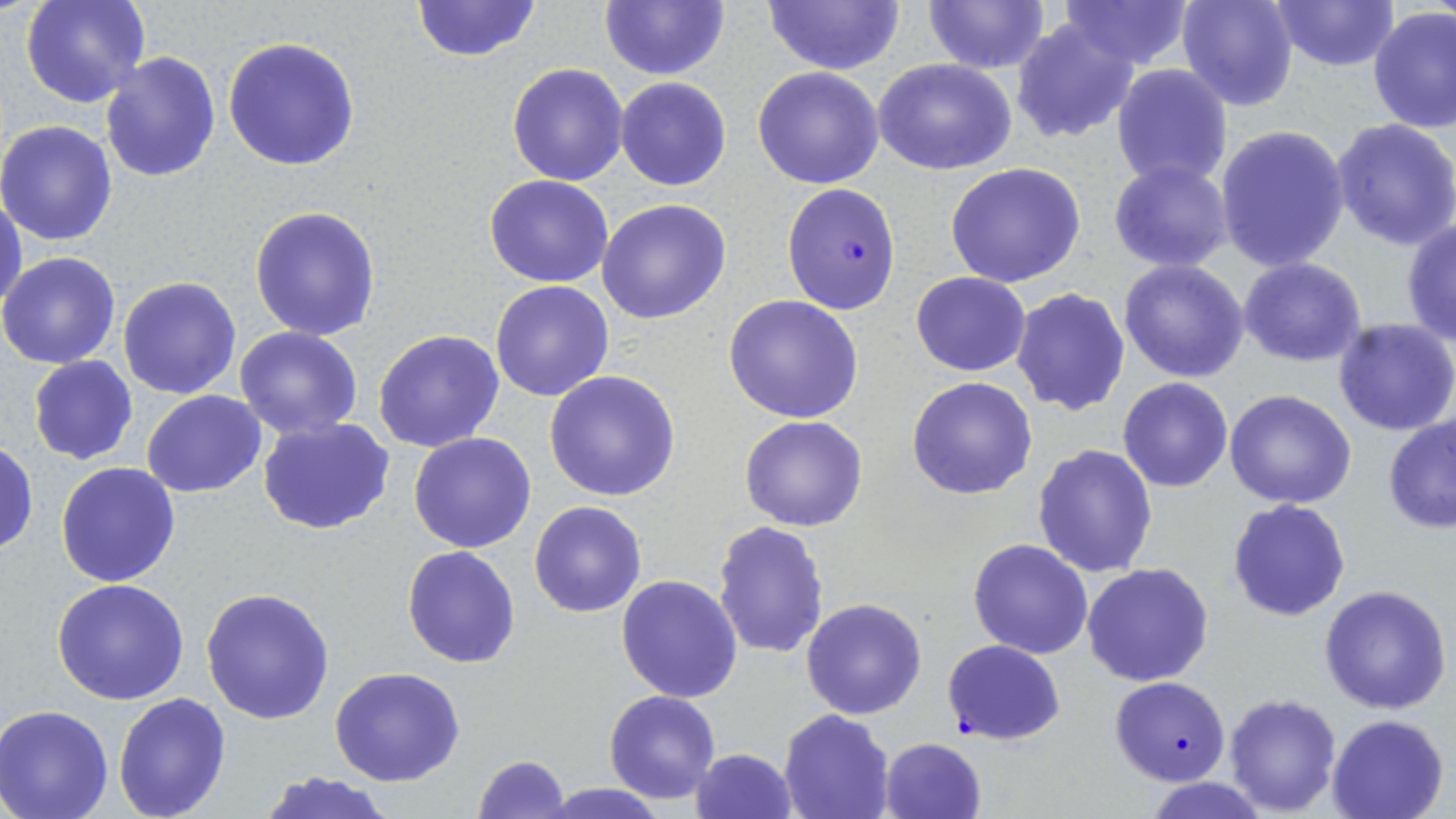
Approximate bounding boxes as named x1/y1/x2/y2 corners in pixels. Uninfected red blood cell locations: (x1=21, y1=0, x2=149, y2=108), (x1=598, y1=0, x2=731, y2=82), (x1=759, y1=0, x2=907, y2=74), (x1=924, y1=0, x2=1052, y2=73), (x1=1054, y1=0, x2=1196, y2=71), (x1=1176, y1=0, x2=1298, y2=112), (x1=1266, y1=0, x2=1402, y2=71), (x1=409, y1=1, x2=545, y2=61), (x1=1369, y1=7, x2=1456, y2=134), (x1=1011, y1=17, x2=1140, y2=144), (x1=223, y1=37, x2=362, y2=172), (x1=99, y1=52, x2=221, y2=182), (x1=873, y1=57, x2=1016, y2=176), (x1=507, y1=61, x2=631, y2=184), (x1=1112, y1=63, x2=1233, y2=189), (x1=753, y1=65, x2=885, y2=188), (x1=615, y1=76, x2=732, y2=192), (x1=1330, y1=118, x2=1456, y2=250), (x1=0, y1=119, x2=120, y2=246), (x1=1215, y1=124, x2=1350, y2=272), (x1=1107, y1=159, x2=1235, y2=272), (x1=945, y1=162, x2=1087, y2=287), (x1=484, y1=174, x2=615, y2=288), (x1=0, y1=189, x2=27, y2=316), (x1=597, y1=198, x2=732, y2=324), (x1=250, y1=206, x2=383, y2=342), (x1=1401, y1=217, x2=1456, y2=346), (x1=0, y1=251, x2=122, y2=368), (x1=1239, y1=256, x2=1367, y2=367), (x1=1118, y1=258, x2=1251, y2=383), (x1=911, y1=272, x2=1031, y2=376), (x1=118, y1=276, x2=242, y2=400), (x1=490, y1=281, x2=614, y2=402), (x1=1011, y1=287, x2=1131, y2=416), (x1=723, y1=295, x2=864, y2=424), (x1=1333, y1=318, x2=1456, y2=437), (x1=234, y1=327, x2=364, y2=441), (x1=373, y1=328, x2=505, y2=453), (x1=28, y1=356, x2=138, y2=464), (x1=544, y1=370, x2=681, y2=502), (x1=907, y1=376, x2=1039, y2=499), (x1=1118, y1=376, x2=1233, y2=492), (x1=1225, y1=389, x2=1357, y2=510), (x1=142, y1=390, x2=266, y2=496), (x1=1382, y1=413, x2=1456, y2=533), (x1=739, y1=414, x2=869, y2=531), (x1=257, y1=417, x2=395, y2=536), (x1=408, y1=433, x2=537, y2=553), (x1=1, y1=438, x2=38, y2=557), (x1=1033, y1=443, x2=1160, y2=578), (x1=56, y1=462, x2=181, y2=587), (x1=1227, y1=498, x2=1351, y2=621), (x1=529, y1=500, x2=648, y2=618), (x1=713, y1=519, x2=831, y2=657), (x1=967, y1=539, x2=1093, y2=658), (x1=402, y1=545, x2=521, y2=667), (x1=1082, y1=562, x2=1214, y2=686), (x1=616, y1=574, x2=743, y2=703), (x1=52, y1=578, x2=190, y2=703), (x1=1319, y1=584, x2=1453, y2=715), (x1=200, y1=586, x2=336, y2=725), (x1=801, y1=598, x2=927, y2=720), (x1=330, y1=667, x2=465, y2=787), (x1=604, y1=689, x2=721, y2=804), (x1=1223, y1=692, x2=1341, y2=814), (x1=114, y1=693, x2=232, y2=819), (x1=0, y1=706, x2=117, y2=819), (x1=779, y1=710, x2=894, y2=819), (x1=1325, y1=713, x2=1450, y2=819), (x1=878, y1=736, x2=987, y2=818), (x1=689, y1=748, x2=798, y2=819), (x1=471, y1=754, x2=570, y2=819), (x1=256, y1=770, x2=398, y2=819), (x1=1147, y1=777, x2=1269, y2=818), (x1=538, y1=783, x2=673, y2=818). Plasmodium falciparum-infected red blood cell locations: (x1=780, y1=181, x2=902, y2=315), (x1=942, y1=639, x2=1065, y2=745), (x1=1109, y1=674, x2=1231, y2=787). Slide-level diagnosis: Plasmodium falciparum. Captured at 1000x magnification. Single field of view. Optical microscopy. Image is 1456×819 pixels. Thin blood film. May-Grünwald-Giemsa-stained preparation.